Assess this cell for malaria.
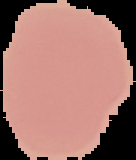
It is uninfected.

Cell region segmented out of the field of view; the surrounding area is masked to black. Image is 136×160 pixels. From a thin blood film.